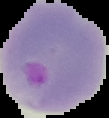

image size = 109×118 pixels
malaria status = parasitized
preparation = thin blood smear
image type = segmented cell region on a black background